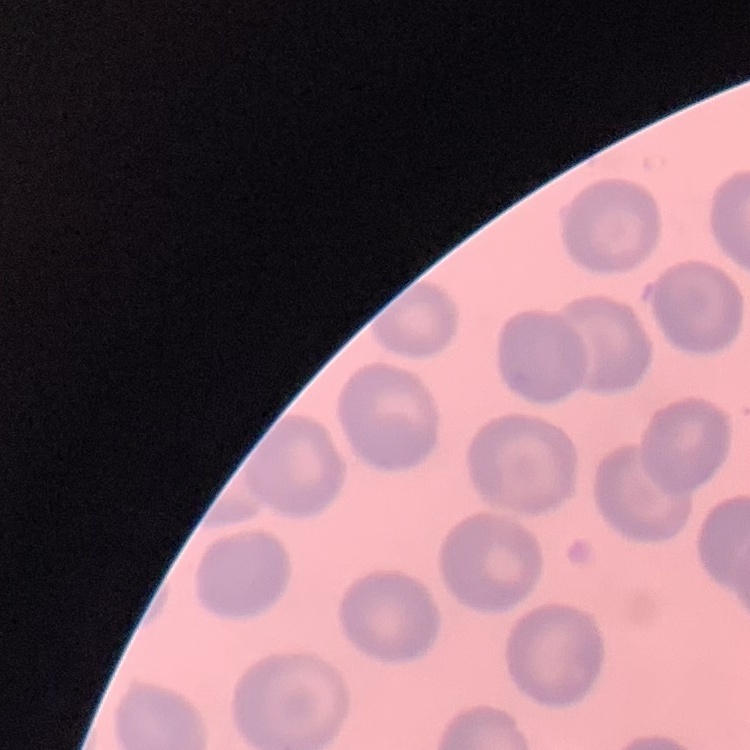

Summary:
  - Erythrocyte morphology: no rouleaux formation
  - Image type: square crop of a larger photomicrograph
  - Stain: Field's or Giemsa
  - Preparation: thin blood film